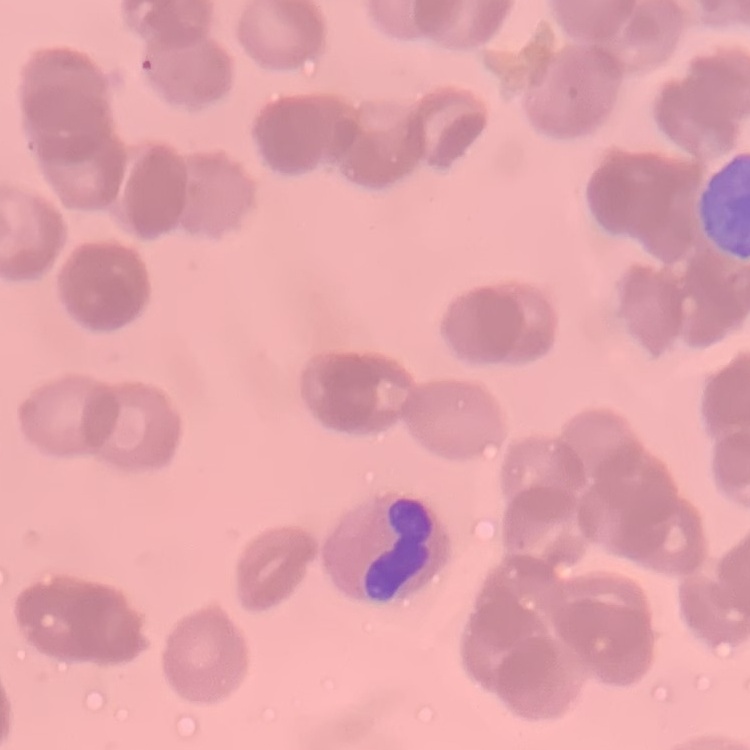

Summary:
  - Erythrocyte morphology: rouleaux formation
  - Image type: square crop of a larger photomicrograph
  - Stain: Field's or Giemsa
  - Preparation: thin blood smear